Identify the cell.
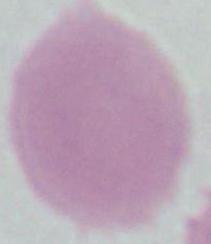

This is an erythrocyte.

Summary:
  - Modality: micrograph
  - Magnification: 1000x